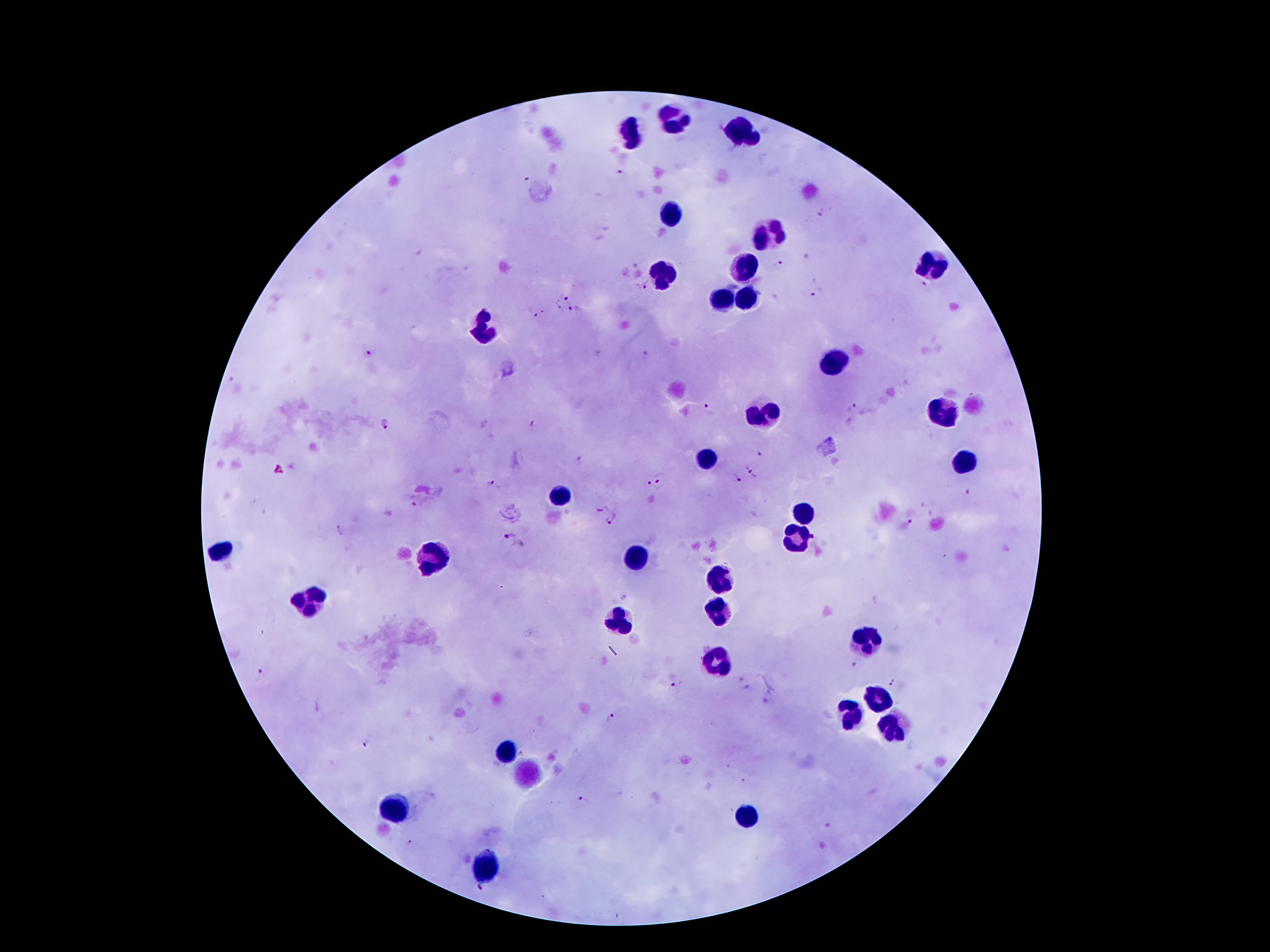
coordinate format = approximate centers as (x, y) in pixels
malaria parasite locations = (620, 176), (823, 215), (779, 264), (643, 285), (926, 287), (818, 295), (562, 298), (574, 311), (538, 314), (368, 354), (851, 408), (709, 410), (384, 424), (533, 427), (760, 455), (752, 469), (661, 476), (733, 479), (491, 484), (651, 492), (968, 494), (415, 504), (911, 515), (614, 519), (508, 539), (856, 665), (260, 675), (893, 683), (677, 687), (745, 689), (611, 717), (367, 745), (582, 801), (409, 842), (479, 888)
leukocyte locations = (671, 122), (742, 133), (632, 134), (667, 214), (769, 236), (932, 263), (744, 272), (665, 278), (744, 296), (718, 300), (477, 329), (835, 365), (941, 413), (764, 415), (707, 457), (961, 464), (561, 494), (804, 511), (795, 541), (220, 550), (634, 555), (435, 558), (722, 580), (307, 601), (716, 614), (618, 621), (866, 641), (716, 662), (875, 701), (853, 714), (888, 724), (506, 753), (393, 810), (749, 815), (488, 866)
field of view = single
preparation = thick peripheral-blood smear
stain = Giemsa
patient malaria status = infected with Plasmodium falciparum
capture = smartphone through the microscope eyepiece
magnification = 100x
image size = 1270×952 pixels